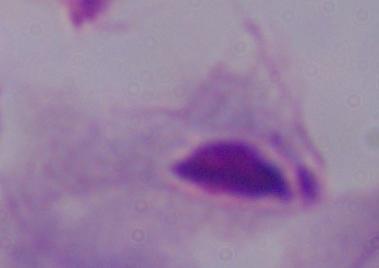

identification = trichomonad
modality = photomicrograph
magnification = 1000x